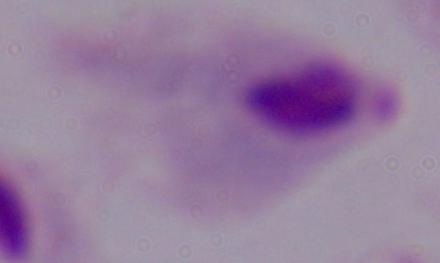
A trichomonad is seen. 1000x magnification. Micrograph.